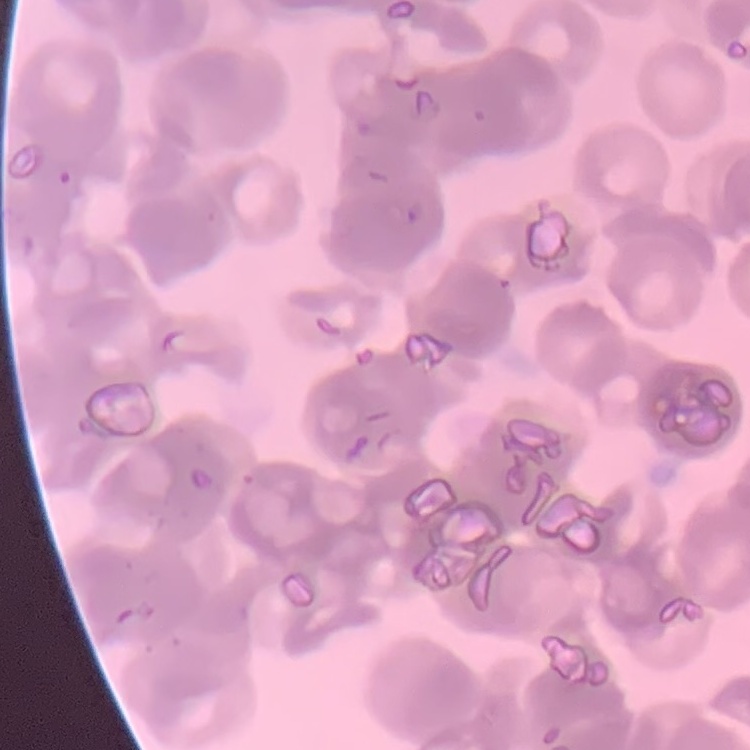
Summary:
  - Erythrocyte morphology: rouleaux formation
  - Stain: Field's or Giemsa
  - Preparation: thin blood smear
  - Image type: one tile cut from a larger photomicrograph